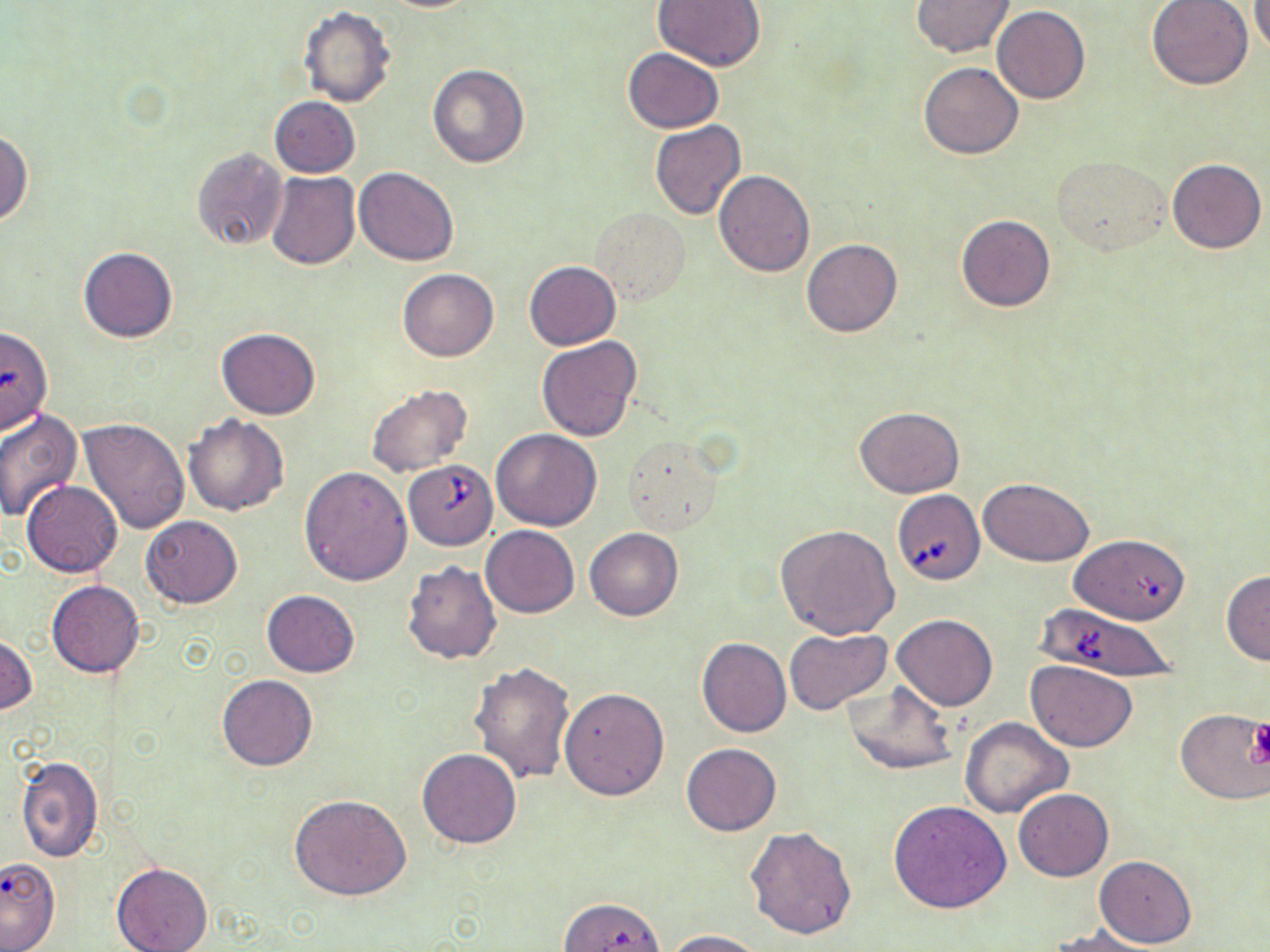
Summary:
  - Coordinate format: approximate bounding boxes as (x1,y1)-(x2,y2) corner pairs in pixels
  - Platelet locations: (1247,720)-(1270,766)
  - Babesia divergens-infected red blood cell locations: (405,460)-(497,547), (892,489)-(985,585), (1060,538)-(1194,632), (1033,607)-(1181,684)
  - Uninfected red blood cell locations: (383,0)-(480,12), (653,0)-(765,73), (1146,0)-(1253,90), (1251,0)-(1269,57), (910,1)-(1016,57), (992,6)-(1090,104), (299,7)-(396,108), (623,48)-(724,132), (919,61)-(1023,160), (427,63)-(530,168), (269,97)-(360,178), (649,121)-(746,221), (0,129)-(33,228), (190,146)-(290,252), (1052,154)-(1169,254), (1167,158)-(1266,253), (355,167)-(459,266), (713,170)-(815,276), (265,171)-(360,269), (591,209)-(691,306), (955,214)-(1055,313), (802,239)-(902,337), (79,247)-(177,343), (524,261)-(621,350), (398,268)-(498,361), (216,329)-(321,419), (536,336)-(644,442), (366,384)-(475,477), (854,406)-(964,498), (0,408)-(84,521), (183,415)-(289,516), (78,417)-(191,534), (491,429)-(602,532), (622,436)-(723,536), (300,467)-(412,586), (978,478)-(1094,565), (22,481)-(122,576), (141,516)-(243,609), (776,524)-(898,639), (480,525)-(579,618), (584,527)-(684,621), (401,559)-(501,665), (1221,570)-(1269,665), (46,581)-(144,678), (261,589)-(359,677), (892,614)-(997,709), (784,627)-(891,716), (0,633)-(37,715), (697,637)-(791,738), (1025,659)-(1139,752), (468,661)-(577,784), (217,675)-(318,770), (844,682)-(959,775), (560,687)-(669,799), (1175,709)-(1270,803), (959,718)-(1073,819), (681,743)-(782,835), (418,749)-(521,848), (16,754)-(102,861), (1013,789)-(1114,882), (289,794)-(412,901), (888,800)-(1012,914), (745,826)-(857,940), (1094,855)-(1197,947), (0,857)-(60,952), (112,863)-(212,952), (558,897)-(666,951), (1048,925)-(1162,952), (662,929)-(763,951)
  - Slide-level diagnosis: Babesia divergens
  - Modality: optical microscopy
  - Preparation: thin blood film
  - Image size: 1270×952 pixels
  - Field of view: single
  - Magnification: 1000x
  - Stain: May-Grünwald-Giemsa